Locate every Plasmodium parasite.
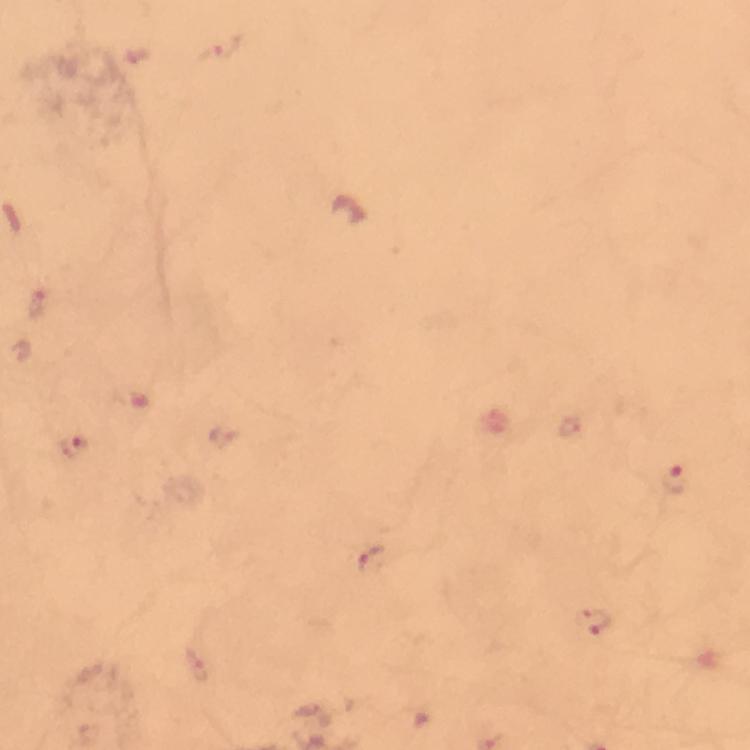
Approximate centers as {x, y} in pixels.
Plasmodium parasites: {226, 47}, {40, 304}, {73, 448}, {673, 480}, {373, 560}, {592, 624}.

Summary:
  - Capture: smartphone mounted on the microscope
  - Magnification: 100x
  - Context: from a malaria diagnostic workup
  - Immersion oil: used
  - Preparation: thick blood film
  - Stain: Giemsa
  - Cropped from: one field of view
  - Image size: 750×750 pixels